Assess this cell for malaria.
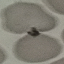

Uninfected.

Acquired by smartphone through the microscope eyepiece. Giemsa stain. Cell patch, automatically extracted from a larger field of view and resized to 64 × 64 pixels. Thin blood smear.